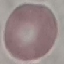

result = negative for malaria parasites
capture = smartphone through the microscope eyepiece
stain = Giemsa
image type = cell patch, automatically extracted from a larger field of view and resized to 64 × 64 pixels
preparation = thin smear